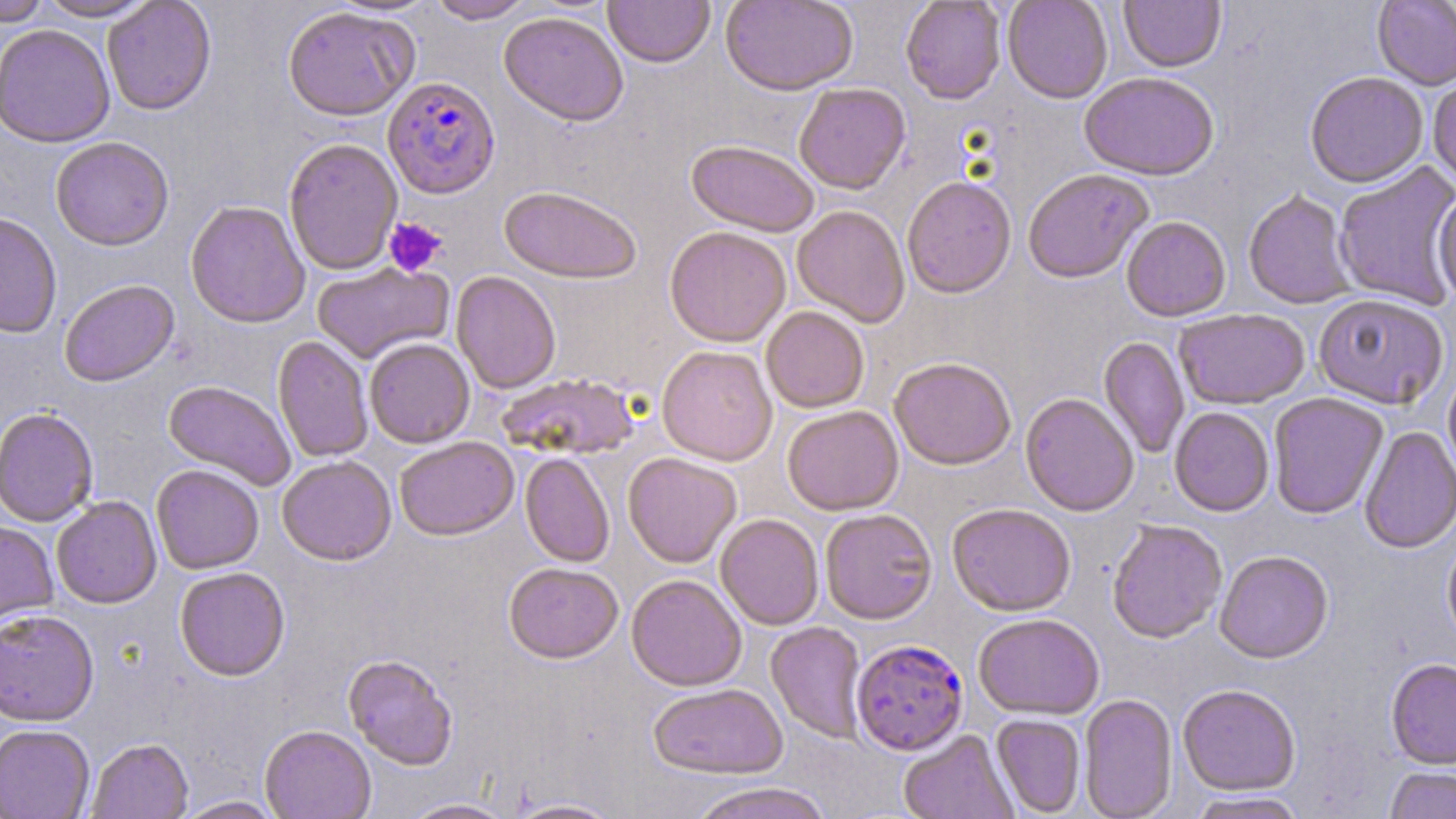
plasmodium_falciparum_infected_red_blood_cell_locations: 'approximate bounding boxes as named x1/y1/x2/y2 corners in pixels: (x1=383, y1=75, x2=500, y2=199), (x1=851, y1=639, x2=969, y2=756)'
slide_level_diagnosis: Plasmodium falciparum
platelet_locations: 'approximate bounding boxes as named x1/y1/x2/y2 corners in pixels: (x1=383, y1=217, x2=447, y2=277)'
image_size: 1456×819 pixels
field_of_view: single
preparation: thin blood smear
uninfected_red_blood_cell_locations: 'approximate bounding boxes as named x1/y1/x2/y2 corners in pixels: (x1=1, y1=0, x2=51, y2=26), (x1=36, y1=0, x2=157, y2=21), (x1=102, y1=0, x2=216, y2=115), (x1=427, y1=0, x2=535, y2=23), (x1=604, y1=0, x2=715, y2=68), (x1=720, y1=0, x2=858, y2=96), (x1=900, y1=0, x2=1006, y2=105), (x1=1002, y1=0, x2=1113, y2=104), (x1=1119, y1=0, x2=1226, y2=74), (x1=1372, y1=0, x2=1456, y2=92), (x1=282, y1=5, x2=418, y2=121), (x1=499, y1=12, x2=629, y2=126), (x1=0, y1=23, x2=115, y2=148), (x1=1305, y1=72, x2=1428, y2=190), (x1=1079, y1=74, x2=1219, y2=183), (x1=1428, y1=77, x2=1456, y2=189), (x1=794, y1=84, x2=911, y2=195), (x1=50, y1=136, x2=174, y2=251), (x1=283, y1=138, x2=402, y2=275), (x1=686, y1=141, x2=819, y2=238), (x1=1335, y1=163, x2=1456, y2=309), (x1=1023, y1=170, x2=1154, y2=285), (x1=902, y1=176, x2=1016, y2=299), (x1=498, y1=186, x2=642, y2=284), (x1=1243, y1=190, x2=1356, y2=310), (x1=1432, y1=191, x2=1456, y2=304), (x1=185, y1=200, x2=310, y2=328), (x1=792, y1=205, x2=910, y2=328), (x1=0, y1=213, x2=62, y2=339), (x1=1121, y1=217, x2=1231, y2=322), (x1=664, y1=226, x2=791, y2=347), (x1=312, y1=262, x2=453, y2=364), (x1=451, y1=271, x2=561, y2=394), (x1=59, y1=279, x2=179, y2=387), (x1=1313, y1=296, x2=1449, y2=411), (x1=761, y1=307, x2=869, y2=413), (x1=1174, y1=309, x2=1310, y2=411), (x1=272, y1=336, x2=373, y2=462), (x1=1098, y1=337, x2=1190, y2=459), (x1=364, y1=338, x2=475, y2=448), (x1=657, y1=345, x2=777, y2=466), (x1=889, y1=358, x2=1016, y2=470), (x1=1443, y1=366, x2=1456, y2=484), (x1=495, y1=374, x2=642, y2=460), (x1=163, y1=380, x2=297, y2=490), (x1=1021, y1=394, x2=1139, y2=517), (x1=1268, y1=394, x2=1388, y2=520), (x1=782, y1=405, x2=904, y2=516), (x1=1169, y1=407, x2=1274, y2=518), (x1=0, y1=408, x2=99, y2=527), (x1=1359, y1=426, x2=1456, y2=555), (x1=394, y1=436, x2=519, y2=540), (x1=520, y1=453, x2=614, y2=567), (x1=623, y1=453, x2=742, y2=568), (x1=277, y1=455, x2=396, y2=565), (x1=151, y1=464, x2=264, y2=574), (x1=51, y1=496, x2=162, y2=609), (x1=947, y1=504, x2=1076, y2=617), (x1=820, y1=509, x2=937, y2=625), (x1=715, y1=514, x2=824, y2=631), (x1=0, y1=520, x2=58, y2=632), (x1=1107, y1=521, x2=1227, y2=645), (x1=1442, y1=534, x2=1456, y2=652), (x1=1214, y1=552, x2=1334, y2=665), (x1=503, y1=562, x2=624, y2=664), (x1=174, y1=567, x2=290, y2=681), (x1=626, y1=574, x2=747, y2=691), (x1=0, y1=609, x2=99, y2=726), (x1=974, y1=614, x2=1104, y2=721), (x1=766, y1=622, x2=868, y2=744), (x1=343, y1=654, x2=458, y2=771), (x1=1385, y1=659, x2=1456, y2=771), (x1=647, y1=684, x2=788, y2=780), (x1=1178, y1=686, x2=1301, y2=797), (x1=1079, y1=694, x2=1177, y2=818), (x1=991, y1=715, x2=1086, y2=817), (x1=0, y1=725, x2=95, y2=819), (x1=260, y1=726, x2=376, y2=819), (x1=898, y1=731, x2=1018, y2=819), (x1=86, y1=739, x2=193, y2=819), (x1=1385, y1=767, x2=1456, y2=818), (x1=687, y1=782, x2=836, y2=819), (x1=1186, y1=792, x2=1308, y2=818), (x1=172, y1=796, x2=286, y2=819), (x1=504, y1=797, x2=626, y2=818), (x1=401, y1=798, x2=518, y2=819)'
modality: light microscopy
stain: May-Grünwald-Giemsa
magnification: 1000x